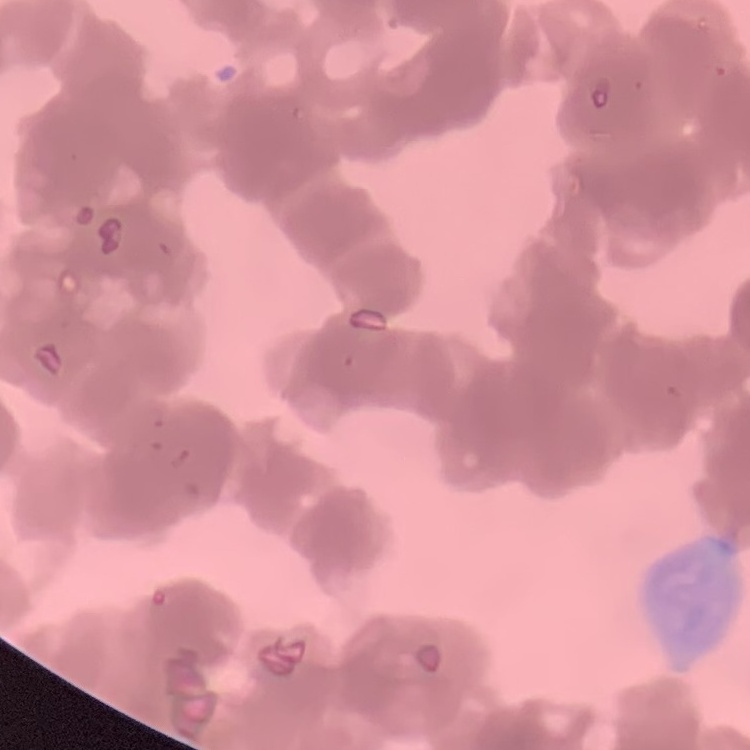
The erythrocytes show rouleaux formation. Thin peripheral smear. Field's or Giemsa stain. One tile cut from a larger photomicrograph.